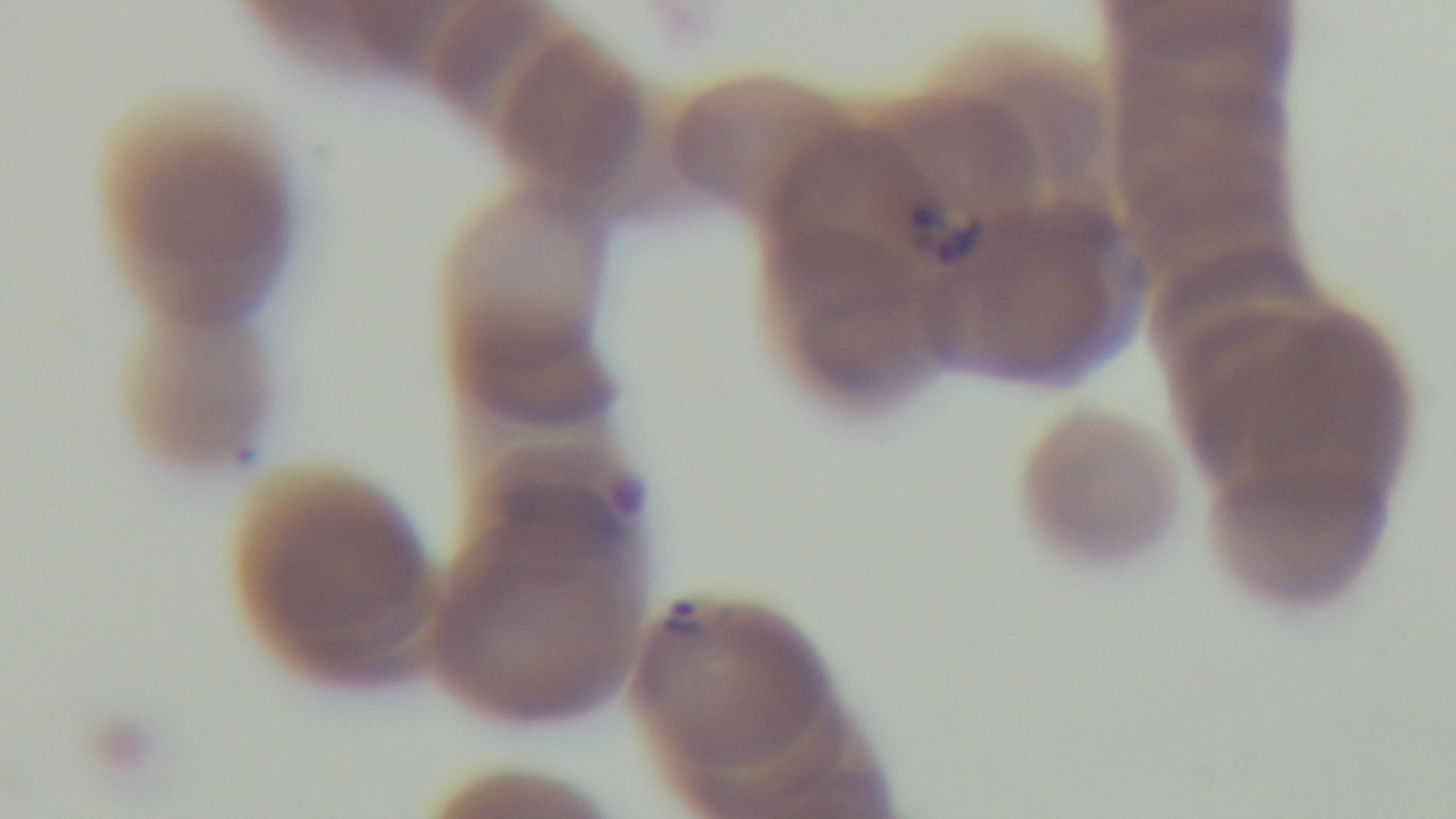

field of view = single
objective = 100x oil immersion
capture = mounted 4K digital camera
stain = Giemsa
malaria status = infected
modality = light microscopy
preparation = thin smear